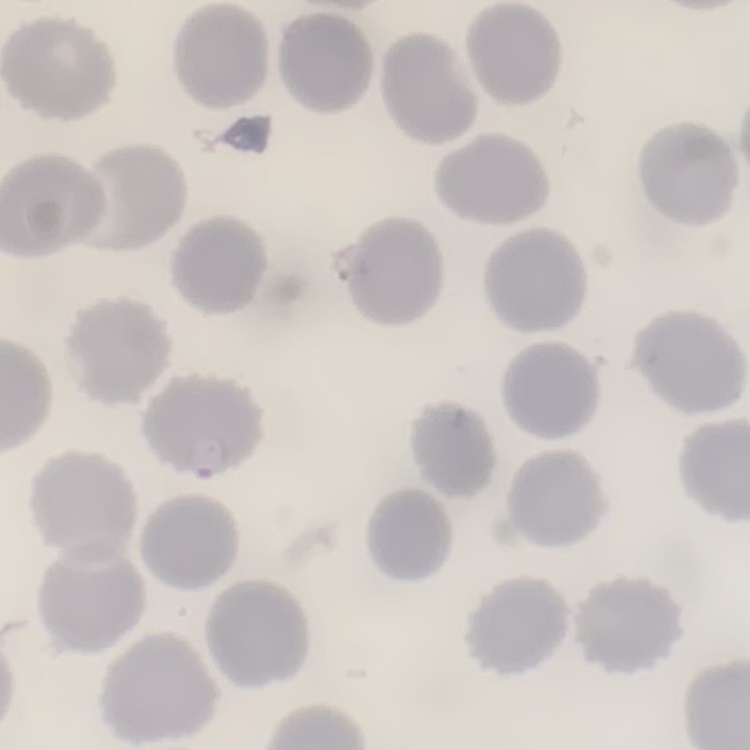
The red blood cells exhibit no rouleaux formation. Square crop of a larger photomicrograph. Stained with either Field's or Giemsa. Thin blood smear.